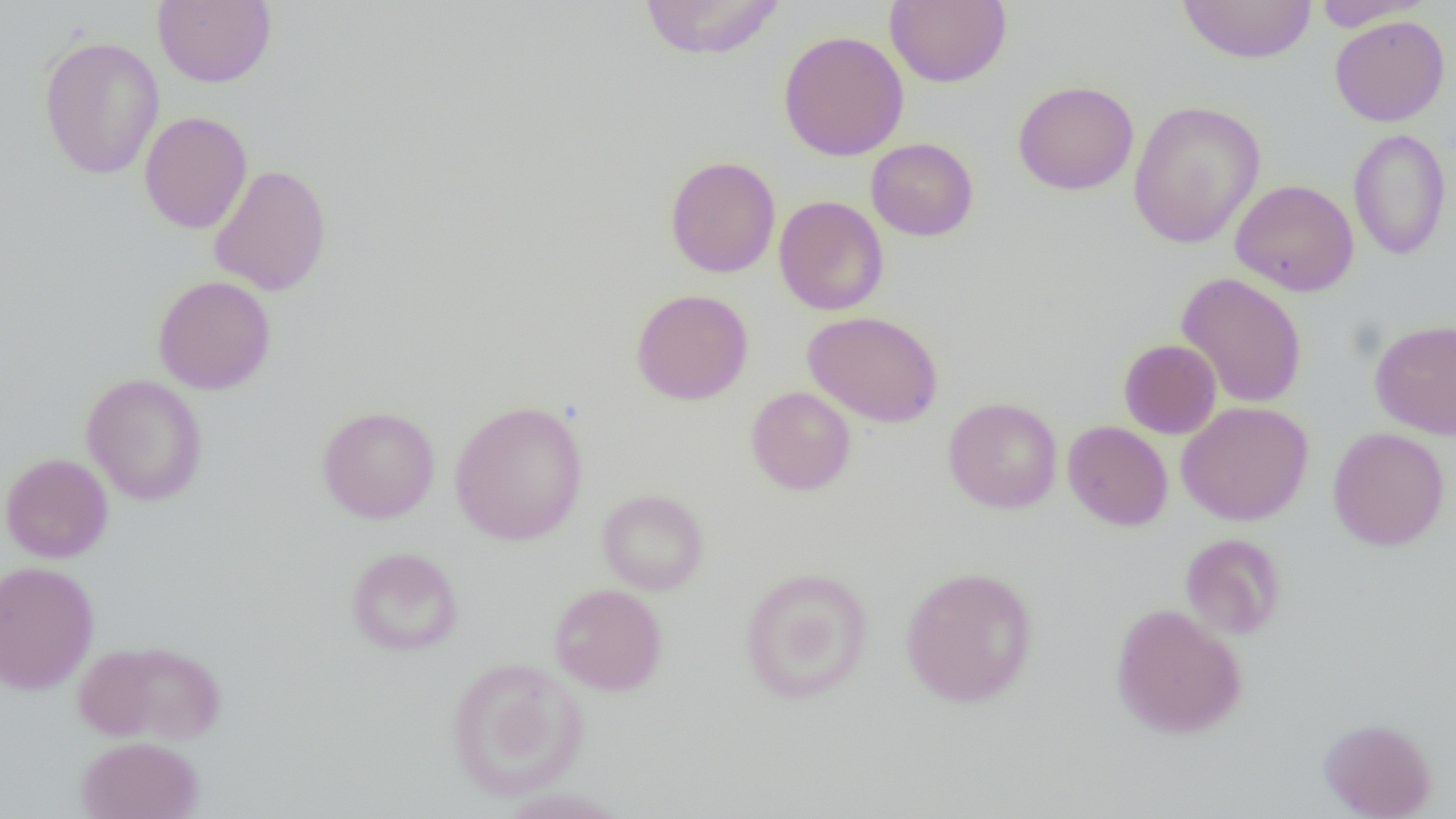

Summary:
  - Coordinate format: approximate bounding boxes as named x1/y1/x2/y2 corners in pixels
  - Uninfected red blood cell locations: (x1=153, y1=0, x2=276, y2=87), (x1=885, y1=0, x2=1011, y2=88), (x1=1177, y1=0, x2=1317, y2=64), (x1=1309, y1=0, x2=1431, y2=31), (x1=637, y1=1, x2=787, y2=60), (x1=1329, y1=15, x2=1449, y2=126), (x1=778, y1=30, x2=909, y2=161), (x1=39, y1=36, x2=165, y2=179), (x1=1013, y1=80, x2=1139, y2=195), (x1=1127, y1=100, x2=1266, y2=249), (x1=139, y1=111, x2=253, y2=234), (x1=1348, y1=128, x2=1452, y2=261), (x1=866, y1=138, x2=979, y2=241), (x1=665, y1=155, x2=780, y2=278), (x1=209, y1=164, x2=332, y2=296), (x1=1230, y1=179, x2=1359, y2=296), (x1=773, y1=195, x2=889, y2=316), (x1=1176, y1=271, x2=1307, y2=408), (x1=152, y1=275, x2=277, y2=395), (x1=630, y1=288, x2=754, y2=405), (x1=803, y1=311, x2=944, y2=428), (x1=1369, y1=318, x2=1456, y2=440), (x1=1118, y1=339, x2=1222, y2=439), (x1=81, y1=374, x2=208, y2=506), (x1=746, y1=386, x2=856, y2=495), (x1=942, y1=397, x2=1063, y2=513), (x1=449, y1=400, x2=589, y2=546), (x1=1176, y1=401, x2=1314, y2=526), (x1=316, y1=405, x2=441, y2=523), (x1=1062, y1=420, x2=1173, y2=531), (x1=1328, y1=427, x2=1450, y2=551), (x1=0, y1=452, x2=114, y2=563), (x1=597, y1=489, x2=708, y2=595), (x1=1180, y1=533, x2=1286, y2=639), (x1=346, y1=546, x2=463, y2=656), (x1=0, y1=559, x2=100, y2=695), (x1=899, y1=565, x2=1039, y2=708), (x1=739, y1=567, x2=874, y2=704), (x1=549, y1=583, x2=667, y2=696), (x1=1110, y1=602, x2=1248, y2=739), (x1=76, y1=639, x2=227, y2=745), (x1=445, y1=657, x2=588, y2=801), (x1=1318, y1=717, x2=1437, y2=818), (x1=76, y1=736, x2=204, y2=818)
  - Slide-level diagnosis: negative for blood parasites
  - Magnification: 1000x
  - Field of view: one of a larger specimen
  - Preparation: thin blood smear
  - Modality: optical microscopy
  - Image size: 1456×819 pixels